Assess this cell for malaria.
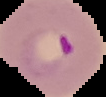
Parasitized.

Cell region segmented out of the field of view; the surrounding area is masked to black. Image is 106×97 pixels. From a thin blood film.